Name the cell type shown.
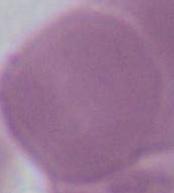

An erythrocyte.

Captured at 1000x magnification. Micrograph.